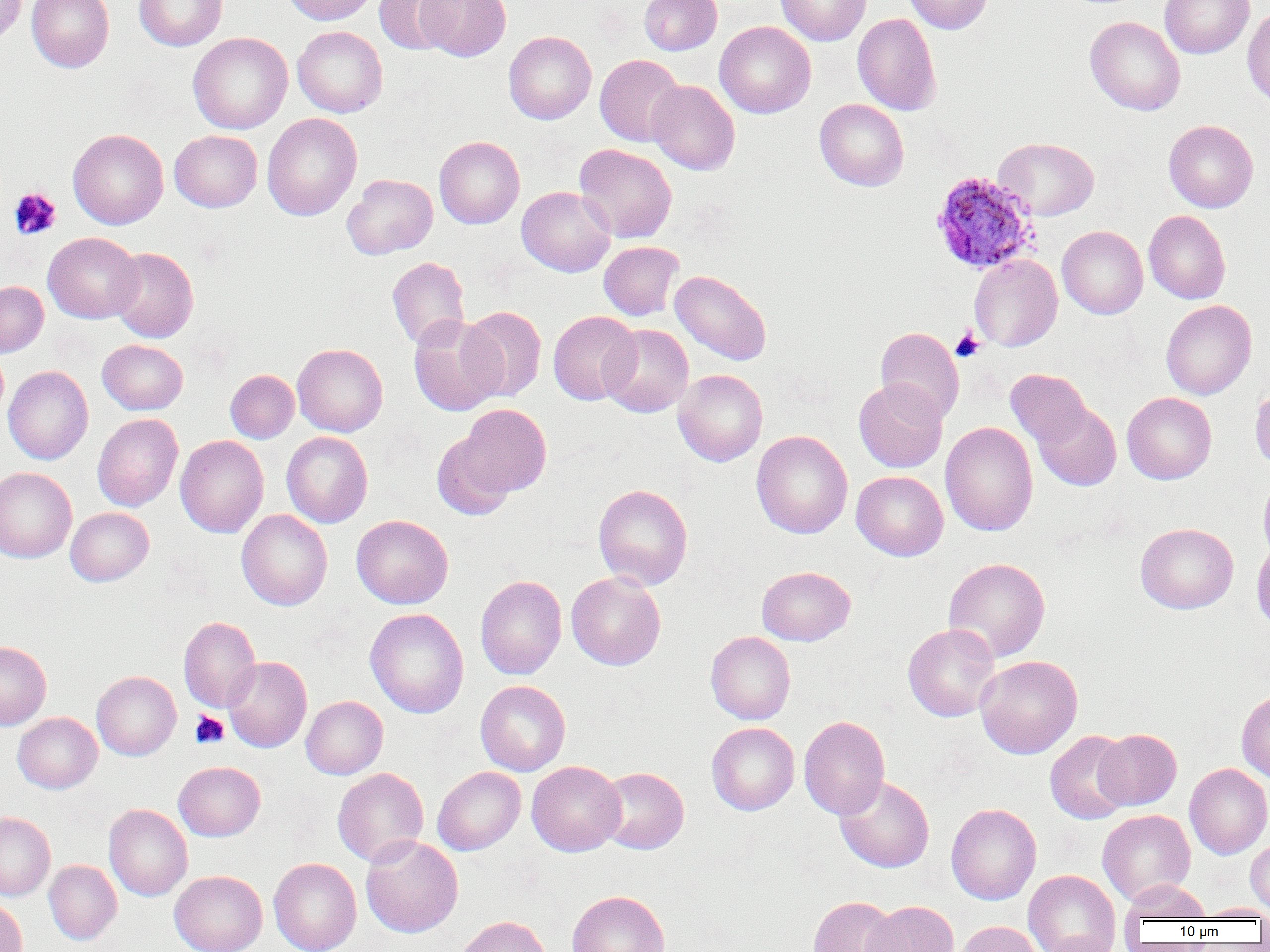
slide_level_diagnosis: Plasmodium ovale
field_of_view: one of a larger specimen
plasmodium_ovale_infected_red_blood_cell_locations: 'approximate bounding boxes as named x1/y1/x2/y2 corners in pixels: (x1=930, y1=169, x2=1040, y2=275)'
image_size: 1270×952 pixels
platelet_locations: 'approximate bounding boxes as named x1/y1/x2/y2 corners in pixels: (x1=8, y1=187, x2=61, y2=240), (x1=951, y1=328, x2=985, y2=362), (x1=190, y1=711, x2=229, y2=749)'
uninfected_red_blood_cell_locations: 'approximate bounding boxes as named x1/y1/x2/y2 corners in pixels: (x1=0, y1=0, x2=26, y2=45), (x1=27, y1=0, x2=114, y2=72), (x1=134, y1=0, x2=227, y2=50), (x1=283, y1=0, x2=378, y2=26), (x1=374, y1=0, x2=459, y2=54), (x1=417, y1=0, x2=511, y2=61), (x1=639, y1=0, x2=721, y2=55), (x1=775, y1=0, x2=871, y2=46), (x1=903, y1=0, x2=993, y2=33), (x1=1160, y1=0, x2=1254, y2=58), (x1=1242, y1=6, x2=1270, y2=109), (x1=852, y1=13, x2=942, y2=115), (x1=1085, y1=16, x2=1185, y2=115), (x1=714, y1=21, x2=816, y2=118), (x1=292, y1=25, x2=388, y2=117), (x1=504, y1=31, x2=596, y2=124), (x1=188, y1=32, x2=292, y2=134), (x1=595, y1=54, x2=685, y2=147), (x1=647, y1=80, x2=740, y2=175), (x1=814, y1=99, x2=909, y2=191), (x1=262, y1=113, x2=362, y2=220), (x1=1163, y1=120, x2=1258, y2=212), (x1=68, y1=129, x2=168, y2=229), (x1=169, y1=130, x2=262, y2=212), (x1=434, y1=136, x2=525, y2=228), (x1=994, y1=137, x2=1100, y2=220), (x1=574, y1=144, x2=677, y2=243), (x1=342, y1=174, x2=437, y2=259), (x1=517, y1=186, x2=615, y2=277), (x1=1143, y1=210, x2=1231, y2=304), (x1=1057, y1=225, x2=1148, y2=319), (x1=43, y1=232, x2=142, y2=323), (x1=599, y1=241, x2=684, y2=320), (x1=107, y1=247, x2=198, y2=342), (x1=969, y1=254, x2=1062, y2=351), (x1=387, y1=256, x2=470, y2=350), (x1=670, y1=270, x2=772, y2=366), (x1=0, y1=281, x2=48, y2=357), (x1=1160, y1=300, x2=1257, y2=400), (x1=459, y1=306, x2=547, y2=402), (x1=548, y1=311, x2=641, y2=405), (x1=408, y1=315, x2=505, y2=416), (x1=600, y1=324, x2=693, y2=417), (x1=875, y1=326, x2=964, y2=424), (x1=98, y1=339, x2=187, y2=414), (x1=292, y1=343, x2=388, y2=436), (x1=0, y1=345, x2=8, y2=425), (x1=3, y1=366, x2=93, y2=464), (x1=1005, y1=369, x2=1093, y2=449), (x1=225, y1=370, x2=299, y2=442), (x1=672, y1=370, x2=768, y2=466), (x1=854, y1=378, x2=948, y2=472), (x1=1250, y1=382, x2=1270, y2=473), (x1=1122, y1=392, x2=1217, y2=484), (x1=1032, y1=399, x2=1121, y2=491), (x1=457, y1=404, x2=551, y2=497), (x1=93, y1=414, x2=183, y2=511), (x1=940, y1=422, x2=1038, y2=536), (x1=751, y1=430, x2=853, y2=538), (x1=282, y1=431, x2=373, y2=528), (x1=432, y1=432, x2=517, y2=520), (x1=175, y1=435, x2=268, y2=537), (x1=0, y1=467, x2=77, y2=563), (x1=851, y1=471, x2=948, y2=561), (x1=1258, y1=474, x2=1270, y2=563), (x1=593, y1=483, x2=693, y2=590), (x1=66, y1=507, x2=154, y2=586), (x1=236, y1=509, x2=332, y2=611), (x1=351, y1=515, x2=453, y2=609), (x1=1135, y1=522, x2=1238, y2=614), (x1=1251, y1=541, x2=1270, y2=634), (x1=943, y1=557, x2=1050, y2=663), (x1=757, y1=566, x2=855, y2=646), (x1=566, y1=571, x2=666, y2=670), (x1=475, y1=575, x2=566, y2=679), (x1=365, y1=608, x2=469, y2=718), (x1=179, y1=616, x2=262, y2=712), (x1=903, y1=623, x2=1001, y2=722), (x1=706, y1=631, x2=796, y2=724), (x1=0, y1=641, x2=51, y2=729), (x1=975, y1=655, x2=1083, y2=759), (x1=223, y1=656, x2=312, y2=752), (x1=92, y1=671, x2=181, y2=760), (x1=475, y1=680, x2=570, y2=775), (x1=1236, y1=689, x2=1270, y2=784), (x1=301, y1=696, x2=388, y2=779), (x1=13, y1=713, x2=102, y2=793), (x1=798, y1=716, x2=890, y2=819), (x1=707, y1=722, x2=799, y2=815), (x1=1093, y1=729, x2=1181, y2=810), (x1=1045, y1=731, x2=1133, y2=824), (x1=526, y1=760, x2=625, y2=856), (x1=173, y1=761, x2=265, y2=841), (x1=1184, y1=763, x2=1270, y2=859), (x1=432, y1=766, x2=526, y2=855), (x1=332, y1=767, x2=429, y2=866), (x1=596, y1=767, x2=689, y2=854), (x1=835, y1=776, x2=934, y2=872), (x1=946, y1=803, x2=1042, y2=905), (x1=104, y1=804, x2=192, y2=901), (x1=1097, y1=809, x2=1195, y2=905), (x1=0, y1=812, x2=55, y2=901), (x1=360, y1=835, x2=463, y2=937), (x1=1245, y1=838, x2=1270, y2=915), (x1=269, y1=857, x2=361, y2=952), (x1=44, y1=860, x2=121, y2=944), (x1=169, y1=870, x2=267, y2=952), (x1=1024, y1=870, x2=1120, y2=951), (x1=1121, y1=879, x2=1210, y2=924), (x1=567, y1=890, x2=669, y2=952), (x1=0, y1=896, x2=27, y2=952), (x1=808, y1=896, x2=901, y2=952), (x1=861, y1=900, x2=959, y2=952), (x1=1197, y1=903, x2=1270, y2=920), (x1=454, y1=915, x2=552, y2=952), (x1=954, y1=921, x2=1043, y2=952), (x1=1041, y1=933, x2=1122, y2=952)'
preparation: thin blood film
modality: light microscopy
magnification: 1000x